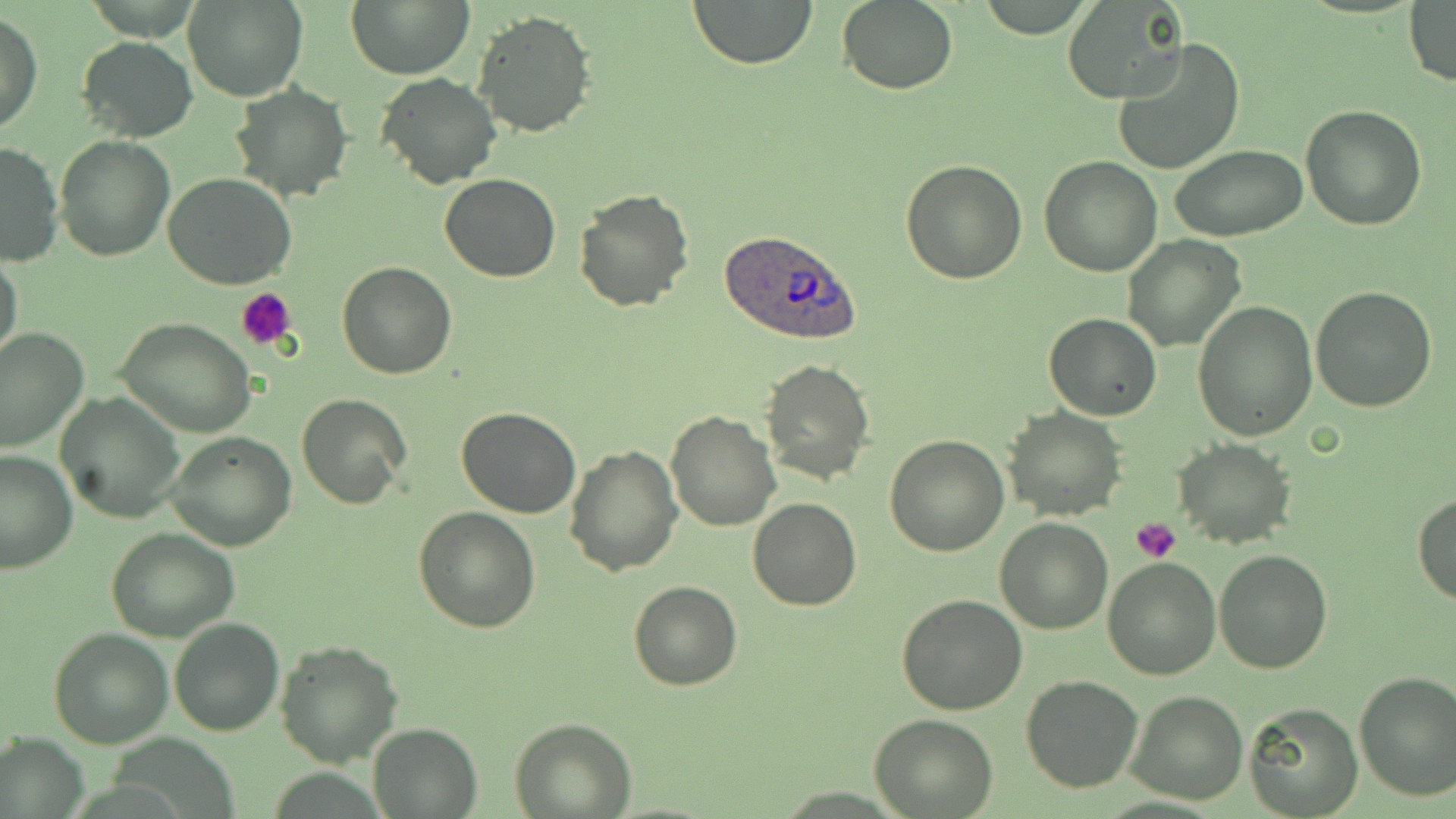

Summary:
  - Coordinate format: approximate bounding boxes as (x1,y1)-(x2,y2) corner pairs in pixels
  - Plasmodium ovale-infected red blood cell locations: (720,227)-(862,344)
  - Uninfected red blood cell locations: (348,0)-(473,78), (689,0)-(818,69), (183,1)-(307,102), (837,1)-(958,95), (1404,1)-(1456,89), (1064,3)-(1184,101), (472,9)-(597,138), (1,10)-(41,135), (1111,35)-(1245,178), (77,36)-(198,142), (375,74)-(501,190), (229,81)-(350,202), (1300,104)-(1428,230), (55,136)-(175,262), (0,141)-(64,267), (1170,144)-(1309,242), (1039,156)-(1162,276), (901,160)-(1029,283), (162,173)-(299,291), (439,174)-(562,282), (572,187)-(694,313), (1123,235)-(1246,351), (0,251)-(24,370), (335,262)-(457,379), (1310,285)-(1437,412), (1193,301)-(1317,443), (1044,312)-(1161,420), (113,317)-(258,439), (0,325)-(90,453), (759,358)-(875,486), (55,392)-(184,522), (297,394)-(411,509), (456,406)-(581,517), (1004,406)-(1126,521), (665,410)-(780,531), (164,431)-(296,552), (884,435)-(1009,556), (1172,440)-(1295,549), (565,442)-(682,575), (0,448)-(77,573), (1414,494)-(1456,606), (747,498)-(861,612), (413,507)-(540,632), (994,516)-(1113,635), (105,526)-(240,641), (1213,549)-(1333,674), (1102,555)-(1219,679), (628,580)-(742,691), (897,595)-(1027,716), (168,617)-(284,736), (49,627)-(174,748), (275,639)-(404,768), (1354,671)-(1456,802), (1020,673)-(1144,793), (1126,690)-(1249,805), (1244,702)-(1363,818), (871,712)-(997,817), (509,718)-(636,818), (366,722)-(481,819), (0,732)-(90,818)
  - Platelet locations: (238,287)-(299,349), (1130,518)-(1182,564)
  - Slide-level diagnosis: Plasmodium ovale
  - Preparation: thin blood smear
  - Field of view: single
  - Modality: light microscopy
  - Magnification: 1000x
  - Stain: May-Grünwald-Giemsa
  - Image size: 1456×819 pixels